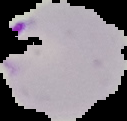
image type = segmented cell region on a black background
preparation = thin blood smear
image size = 127×121 pixels
result = malaria parasites identified